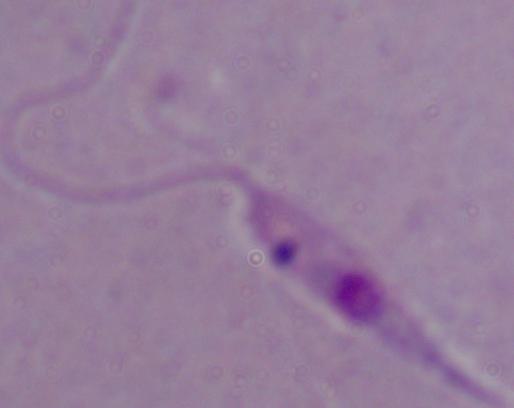 Photomicrograph. Captured at 1000x magnification. A Leishmania parasite is shown.